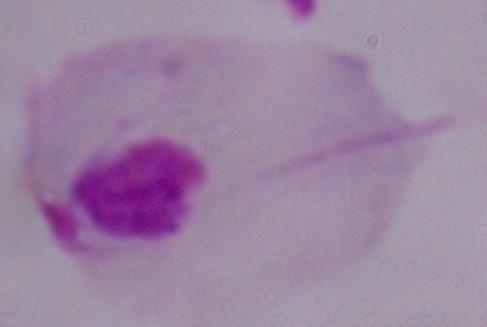

modality = micrograph
magnification = 1000x
identification = trichomonad